Point out every malaria parasite and every leukocyte.
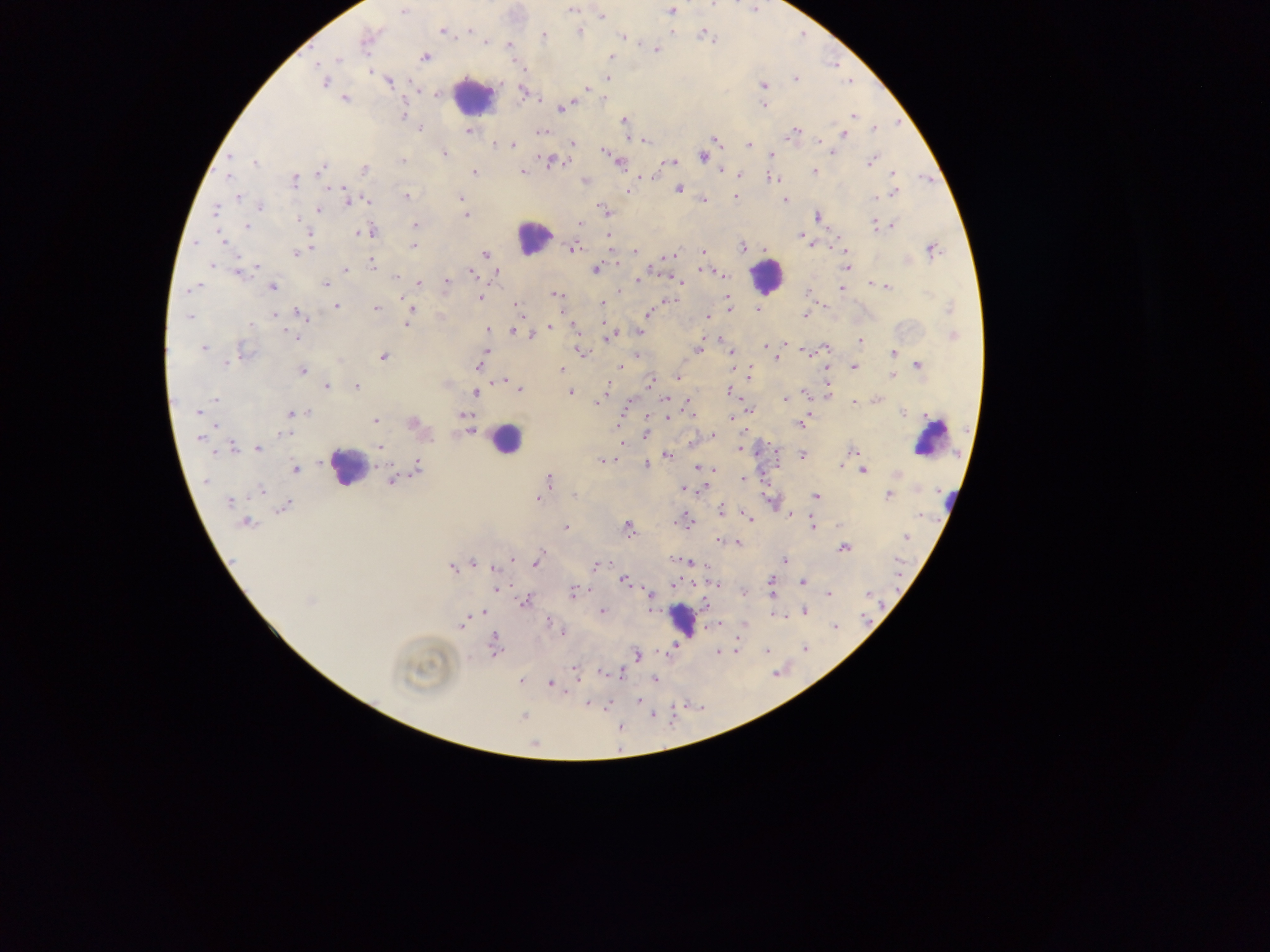
Approximate centers as {x, y} in pixels.
Malaria parasites: {572, 10}, {670, 10}, {403, 12}, {601, 17}, {470, 29}, {669, 29}, {442, 30}, {580, 31}, {704, 35}, {543, 36}, {622, 37}, {367, 38}, {710, 39}, {487, 42}, {509, 45}, {656, 49}, {423, 57}, {610, 58}, {336, 59}, {318, 65}, {523, 67}, {370, 71}, {607, 78}, {796, 78}, {324, 81}, {389, 81}, {763, 85}, {586, 89}, {523, 90}, {437, 92}, {345, 98}, {603, 98}, {763, 105}, {560, 106}, {403, 115}, {853, 116}, {623, 121}, {420, 129}, {874, 129}, {470, 130}, {541, 132}, {793, 133}, {842, 133}, {642, 139}, {713, 139}, {818, 140}, {573, 143}, {496, 145}, {512, 145}, {749, 146}, {605, 150}, {831, 152}, {444, 153}, {703, 156}, {771, 156}, {871, 160}, {402, 161}, {551, 161}, {618, 161}, {253, 162}, {670, 162}, {664, 163}, {364, 169}, {320, 170}, {721, 170}, {812, 170}, {474, 172}, {521, 172}, {739, 174}, {892, 174}, {640, 177}, {228, 178}, {774, 178}, {295, 180}, {585, 181}, {679, 188}, {893, 193}, {237, 196}, {406, 196}, {735, 197}, {460, 198}, {875, 198}, {349, 199}, {365, 200}, {701, 200}, {782, 200}, {258, 206}, {216, 210}, {319, 210}, {605, 211}, {465, 215}, {817, 216}, {298, 218}, {875, 222}, {581, 224}, {893, 225}, {249, 226}, {416, 226}, {365, 231}, {800, 235}, {311, 236}, {608, 236}, {222, 241}, {814, 244}, {413, 246}, {741, 246}, {572, 247}, {764, 249}, {931, 249}, {843, 250}, {635, 251}, {702, 251}, {297, 252}, {485, 254}, {670, 256}, {666, 257}, {907, 259}, {371, 262}, {211, 266}, {255, 266}, {846, 267}, {595, 269}, {346, 270}, {708, 270}, {471, 271}, {239, 272}, {721, 273}, {495, 274}, {397, 276}, {639, 280}, {679, 280}, {445, 282}, {868, 282}, {417, 283}, {326, 284}, {271, 286}, {886, 287}, {189, 289}, {841, 289}, {619, 290}, {807, 290}, {555, 295}, {478, 296}, {669, 299}, {726, 299}, {402, 301}, {337, 305}, {515, 305}, {601, 306}, {376, 307}, {412, 309}, {728, 309}, {758, 309}, {950, 309}, {274, 314}, {647, 314}, {804, 314}, {299, 315}, {708, 315}, {188, 317}, {408, 320}, {604, 322}, {573, 327}, {549, 328}, {512, 330}, {487, 331}, {638, 331}, {296, 336}, {532, 336}, {953, 336}, {607, 337}, {719, 337}, {860, 341}, {764, 345}, {784, 345}, {203, 347}, {825, 347}, {698, 350}, {242, 351}, {581, 351}, {806, 351}, {486, 352}, {731, 352}, {894, 353}, {638, 354}, {383, 355}, {483, 359}, {775, 360}, {226, 361}, {917, 365}, {480, 366}, {620, 366}, {853, 367}, {825, 368}, {561, 369}, {733, 369}, {302, 370}, {749, 375}, {893, 375}, {677, 377}, {502, 380}, {649, 382}, {444, 383}, {326, 386}, {356, 387}, {519, 390}, {606, 390}, {569, 391}, {476, 392}, {729, 392}, {825, 393}, {805, 394}, {664, 398}, {784, 399}, {216, 400}, {688, 400}, {858, 400}, {877, 400}, {599, 401}, {854, 402}, {748, 410}, {198, 412}, {307, 412}, {291, 413}, {902, 413}, {464, 415}, {924, 415}, {645, 416}, {667, 416}, {693, 416}, {731, 418}, {804, 420}, {375, 421}, {412, 423}, {800, 423}, {470, 430}, {285, 433}, {645, 433}, {712, 435}, {201, 436}, {620, 443}, {691, 443}, {233, 447}, {379, 447}, {740, 448}, {258, 449}, {853, 449}, {775, 452}, {665, 455}, {801, 455}, {601, 460}, {775, 464}, {645, 465}, {840, 465}, {697, 468}, {294, 470}, {712, 470}, {862, 470}, {415, 471}, {896, 474}, {742, 478}, {393, 479}, {549, 480}, {207, 481}, {684, 488}, {704, 488}, {260, 490}, {575, 495}, {888, 495}, {815, 496}, {537, 498}, {230, 501}, {285, 506}, {721, 511}, {790, 514}, {920, 516}, {748, 518}, {245, 522}, {684, 522}, {838, 525}, {627, 527}, {812, 527}, {566, 528}, {906, 537}, {720, 540}, {730, 542}, {736, 542}, {844, 548}, {512, 557}, {784, 560}, {537, 561}, {675, 561}, {688, 562}, {601, 563}, {474, 564}, {594, 565}, {452, 566}, {624, 580}, {803, 582}, {672, 583}, {717, 584}, {771, 584}, {496, 589}, {743, 591}, {867, 592}, {573, 593}, {827, 593}, {650, 594}, {772, 594}, {525, 600}, {704, 604}, {484, 612}, {602, 612}, {805, 612}, {775, 614}, {786, 615}, {464, 620}, {547, 620}, {717, 624}, {743, 624}, {836, 626}, {562, 632}, {494, 645}, {675, 647}, {805, 648}, {736, 650}, {766, 650}, {717, 652}, {636, 654}, {575, 670}, {603, 672}, {620, 674}, {654, 678}, {520, 681}, {551, 683}, {567, 694}, {638, 701}, {588, 703}, {607, 707}, {653, 715}, {524, 716}, {620, 728}.
Leukocytes: {472, 95}, {533, 238}, {766, 277}, {505, 438}, {930, 438}, {347, 468}, {951, 501}, {682, 620}.

Summary:
  - Image size: 1270×952 pixels
  - Capture: mobile-phone photograph through a microscope
  - Preparation: thick blood smear
  - Field of view: single
  - Country: Ghana